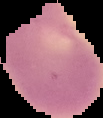 From a thin blood smear. Result: negative for Plasmodium parasites. The area outside the segmented cell region is set to black. Image is 103×118 pixels.